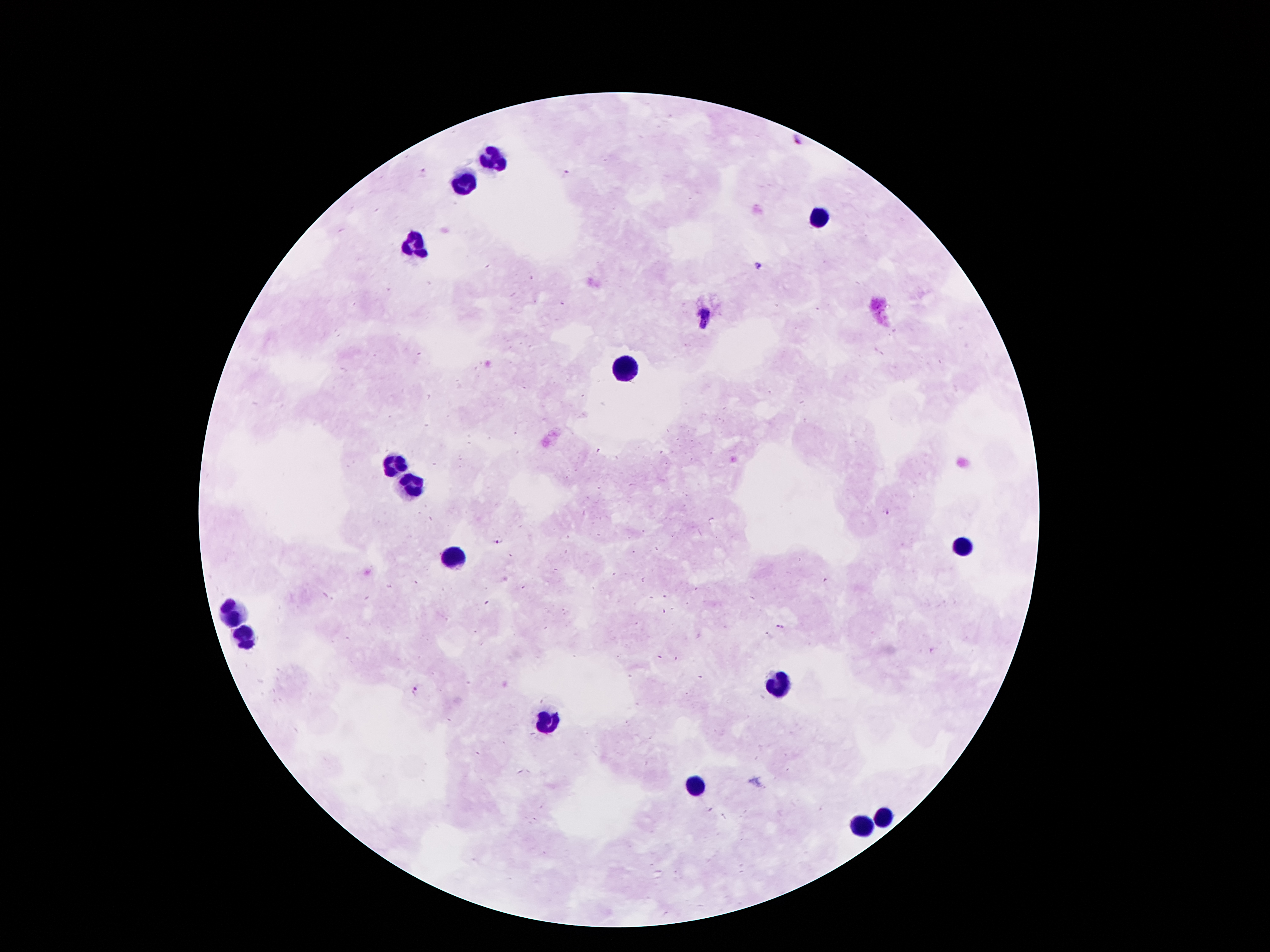

coordinate format = approximate centers as {x, y} in pixels
leukocyte locations = {492, 159}, {463, 182}, {822, 215}, {414, 241}, {626, 366}, {396, 464}, {409, 482}, {965, 545}, {452, 559}, {232, 612}, {247, 640}, {782, 686}, {545, 722}, {694, 786}, {884, 817}, {860, 826}
Plasmodium parasite locations = {797, 141}, {567, 173}, {758, 266}, {706, 313}, {704, 325}, {887, 513}, {496, 543}, {781, 626}, {766, 633}, {932, 651}, {416, 690}
capture = smartphone camera through the microscope eyepiece
stain = Giemsa
preparation = thick blood film
patient malaria status = positive for Plasmodium falciparum
image size = 1270×952 pixels
field of view = single
magnification = 100x